Locate and identify every blood parasite.
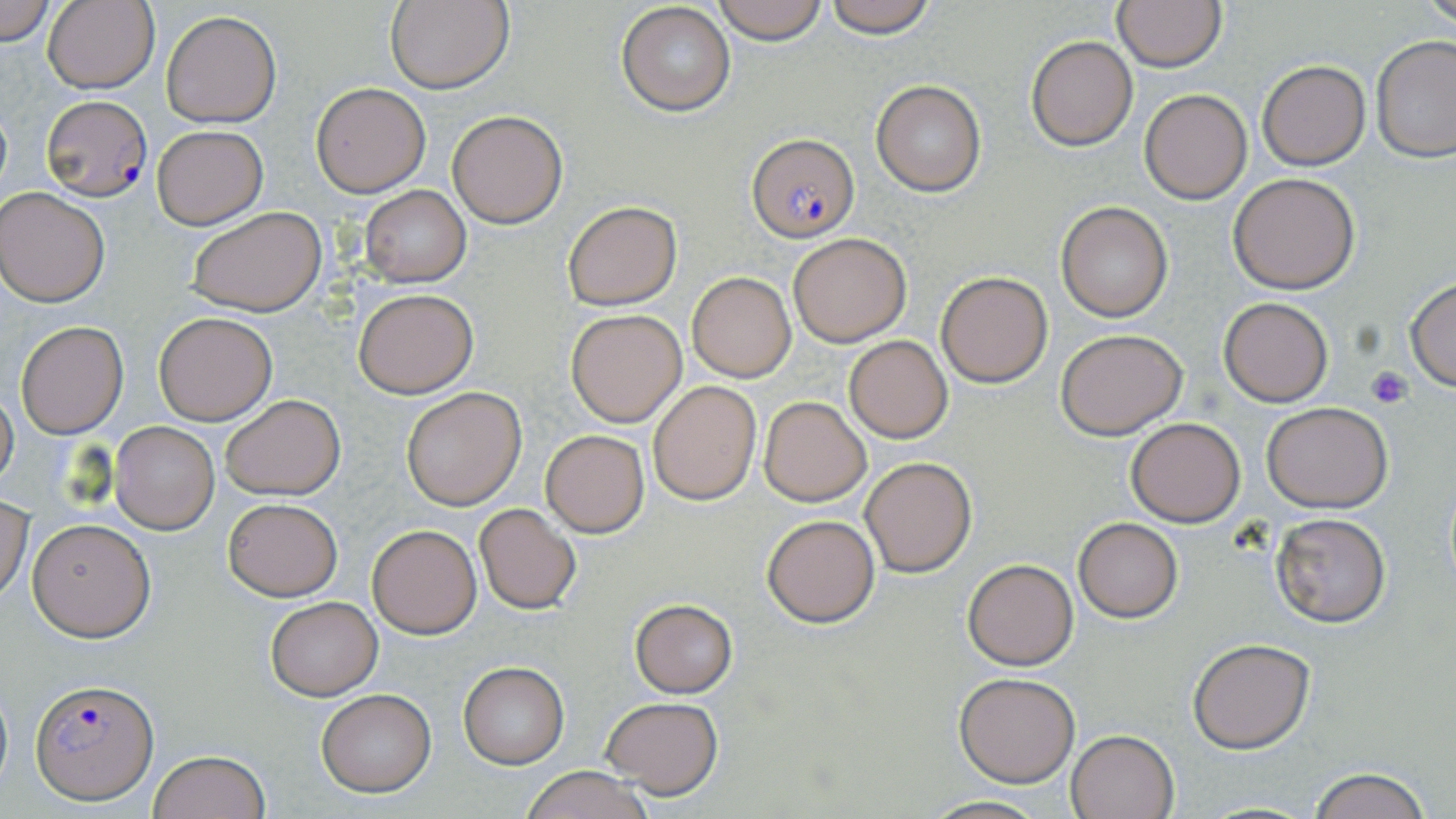

Approximate bounding boxes as (x1,y1)-(x2,y2) corner pairs in pixels.
Plasmodium falciparum-infected red blood cells: (42,94)-(152,201), (747,134)-(859,242), (32,680)-(158,804).
No Plasmodium ovale, Plasmodium malariae, Plasmodium vivax, Babesia divergens, or Trypanosoma brucei observed.

Platelet locations: (1365,366)-(1413,406). Uninfected red blood cell locations: (0,0)-(56,46), (43,0)-(160,94), (385,0)-(512,94), (710,0)-(832,45), (820,0)-(939,38), (1421,0)-(1455,32), (1112,1)-(1226,71), (616,2)-(736,117), (161,9)-(282,128), (1025,34)-(1138,151), (1371,35)-(1456,162), (1257,60)-(1371,170), (871,80)-(986,196), (311,82)-(430,197), (1138,89)-(1253,204), (446,109)-(568,229), (151,125)-(267,229), (1228,173)-(1360,294), (358,184)-(471,288), (0,187)-(110,308), (563,201)-(681,312), (1056,202)-(1174,322), (187,206)-(327,317), (787,232)-(910,347), (685,271)-(796,382), (936,271)-(1052,387), (1404,278)-(1456,392), (353,287)-(478,399), (1218,296)-(1334,406), (565,309)-(687,426), (153,312)-(278,426), (15,319)-(128,439), (1055,327)-(1189,441), (843,335)-(954,443), (648,381)-(760,504), (401,386)-(527,511), (0,388)-(18,492), (220,394)-(345,500), (758,396)-(870,506), (1262,401)-(1393,512), (1125,418)-(1247,527), (110,421)-(220,535), (540,429)-(649,537), (859,456)-(978,576), (0,493)-(33,601), (223,497)-(343,601), (473,503)-(581,613), (1270,511)-(1392,628), (762,513)-(880,628), (28,517)-(156,641), (1074,517)-(1183,622), (367,524)-(481,638), (962,558)-(1078,670), (265,596)-(383,701), (629,598)-(740,698), (1187,638)-(1314,753), (458,661)-(569,768), (954,673)-(1081,787), (0,675)-(12,797), (315,686)-(437,797), (599,695)-(725,799), (1066,728)-(1180,819), (149,748)-(270,819), (1306,766)-(1432,819), (520,767)-(655,819), (919,794)-(1054,818). Slide-level diagnosis: Plasmodium falciparum. Thin blood film. Optical microscopy. May-Grünwald-Giemsa stain. Captured at 1000x magnification. One field of a larger specimen. Image is 1456×819 pixels.